Assess this cell for malaria.
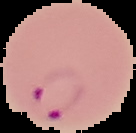

Parasitized.

Segmented cell region on a black background. From a thin blood smear. Image is 136×133 pixels.